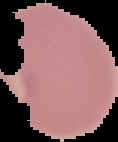
Summary:
  - Preparation: thin blood film
  - Result: Plasmodium parasites detected
  - Image type: segmented cell region with the area outside set to black
  - Image size: 118×142 pixels